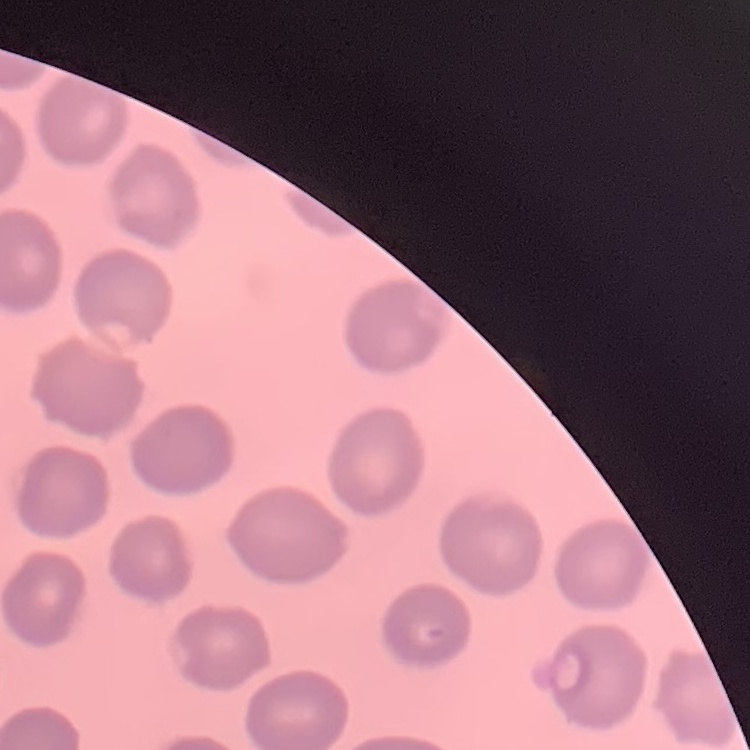

red blood cell morphology = no rouleaux formation
stain = Field's or Giemsa
image type = one tile cut from a larger photomicrograph
preparation = thin peripheral smear